Give the position of every Plasmodium parasite.
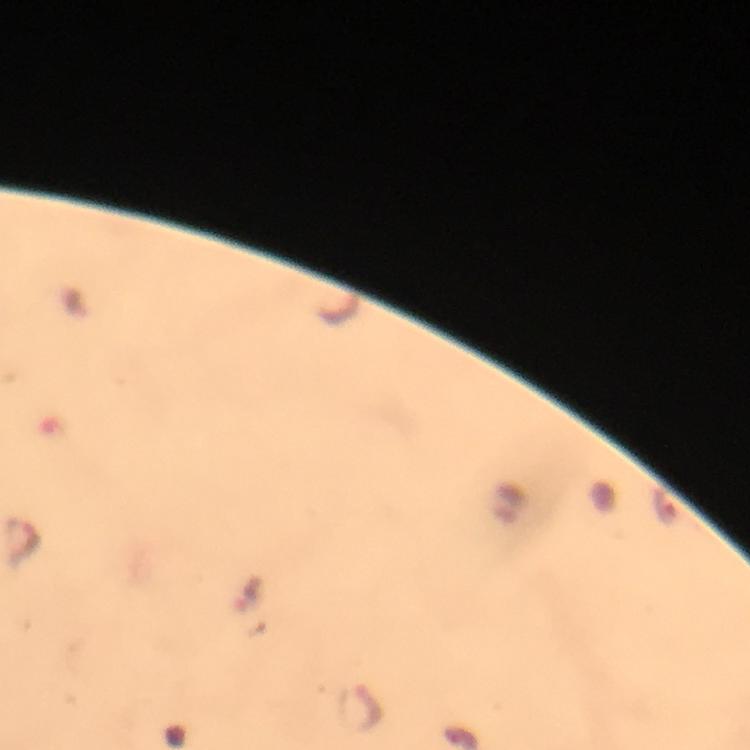

Approximate centers as {x, y} in pixels.
Plasmodium parasites: {25, 543}, {361, 706}.

Summary:
  - Stain: Giemsa
  - Image size: 750×750 pixels
  - Capture: smartphone camera through the microscope
  - Cropped from: a single field of view
  - Preparation: thick smear
  - Context: from a diagnostic examination for malaria
  - Magnification: 100x
  - Immersion oil: applied